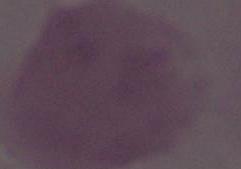

Summary:
  - Modality: photomicrograph
  - Identification: red blood cell
  - Magnification: 1000x